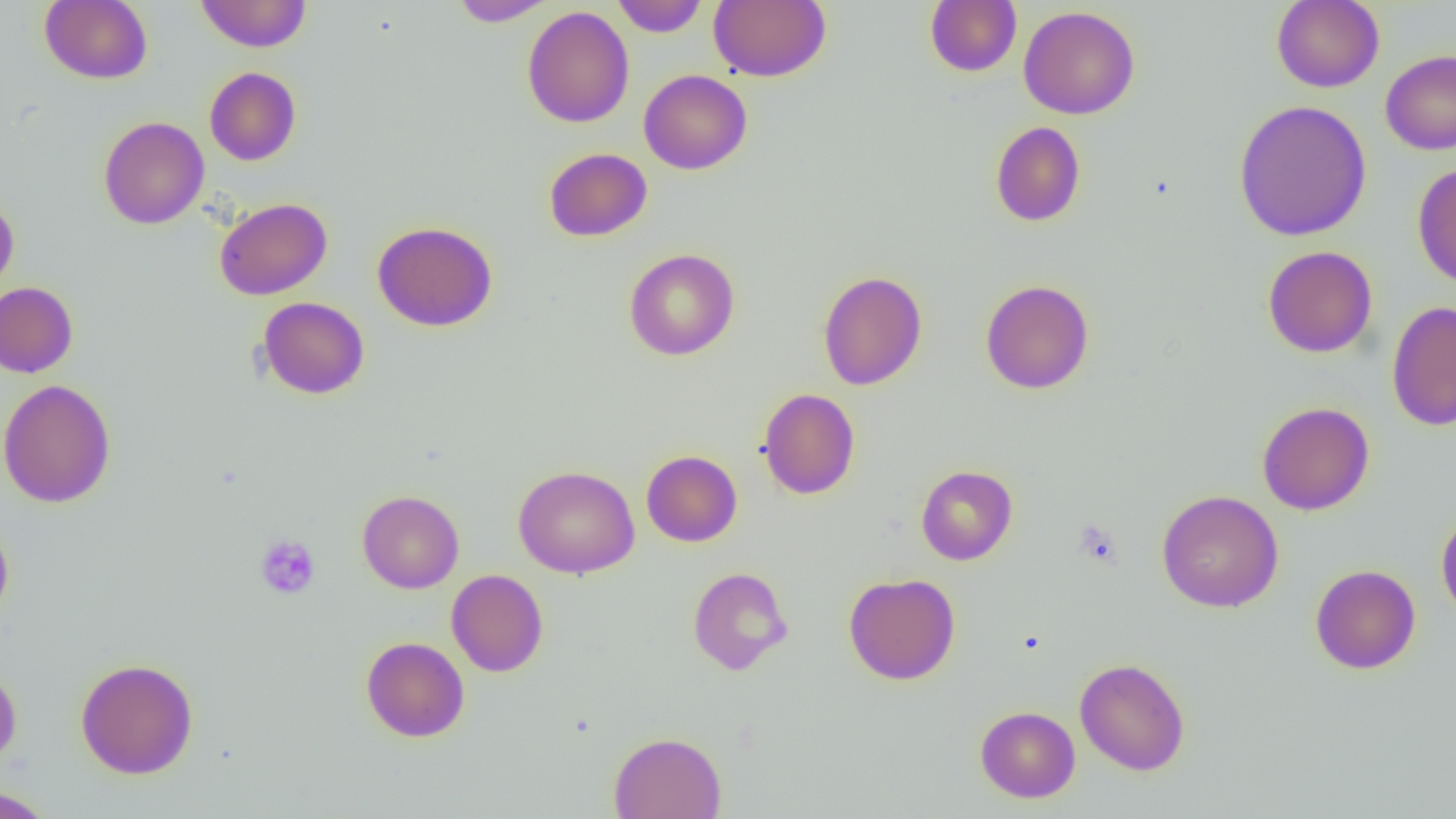 Approximate bounding boxes as (x1,y1)-(x2,y2) corner pairs in pixels. Platelet locations: (1073,518)-(1123,569), (255,535)-(320,599). Uninfected red blood cell locations: (40,0)-(152,84), (195,0)-(311,52), (448,0)-(556,26), (612,0)-(708,37), (709,0)-(831,82), (924,0)-(1022,77), (1271,0)-(1385,92), (521,6)-(634,128), (1018,6)-(1140,120), (1380,50)-(1456,154), (205,67)-(301,166), (639,69)-(752,175), (1233,100)-(1372,242), (98,116)-(209,229), (990,121)-(1086,227), (543,148)-(652,242), (1412,161)-(1456,288), (0,195)-(19,297), (214,197)-(332,300), (372,221)-(498,332), (1262,245)-(1378,358), (624,248)-(740,360), (818,270)-(927,390), (980,279)-(1095,394), (0,281)-(78,378), (257,296)-(370,400), (1386,301)-(1456,431), (0,379)-(116,508), (758,388)-(860,500), (1257,401)-(1374,515), (641,450)-(742,547), (513,465)-(640,579), (916,465)-(1018,565), (1156,489)-(1284,613), (357,490)-(464,593), (1435,507)-(1456,627), (0,519)-(14,625), (1310,564)-(1421,674), (687,567)-(794,675), (446,569)-(549,677), (843,572)-(960,685), (361,637)-(469,742), (1075,657)-(1190,775), (75,658)-(198,779), (0,662)-(22,769), (975,706)-(1080,803), (609,731)-(726,818), (0,786)-(57,818). Slide-level diagnosis: negative for blood parasites. 1000x magnification. Light microscopy. Thin blood film. Image is 1456×819 pixels. Single field of view.